Report the malaria status of this cell.
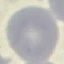
It is uninfected.

Cell patch, automatically extracted from a larger field of view and resized to 64 × 64 pixels. Thin blood smear. Giemsa stain. Acquired by smartphone through the microscope eyepiece.